Assess for malaria.
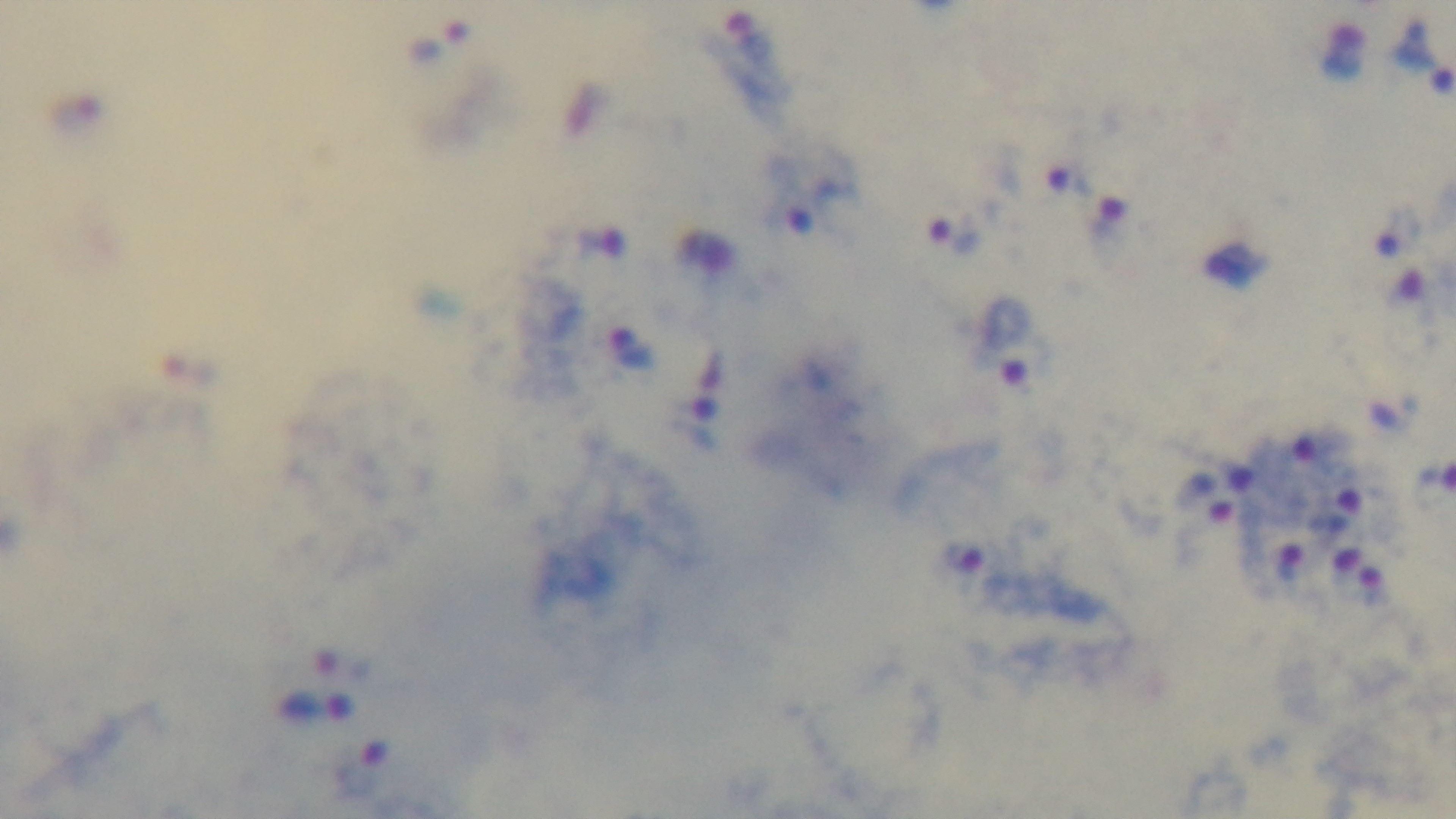

Infected.

Summary:
  - Objective: 100x oil immersion
  - Capture: mounted 4K digital camera
  - Modality: light microscopy
  - Field of view: one from the slide
  - Stain: Giemsa
  - Preparation: thick blood film